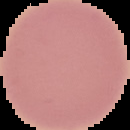

Summary:
  - Image type: segmented cell region on a black background
  - Image size: 130×130 pixels
  - Result: no malaria parasites seen
  - Preparation: thin blood smear